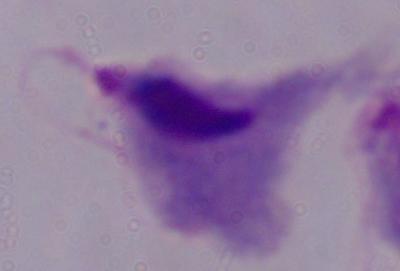

Summary:
  - Identification: trichomonad
  - Magnification: 1000x
  - Modality: photomicrograph